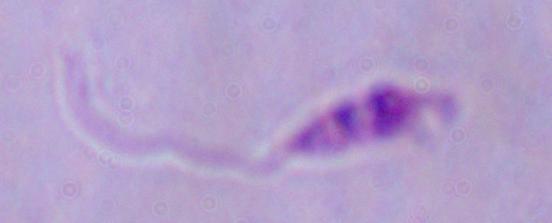

magnification = 1000x
modality = micrograph
identification = Leishmania